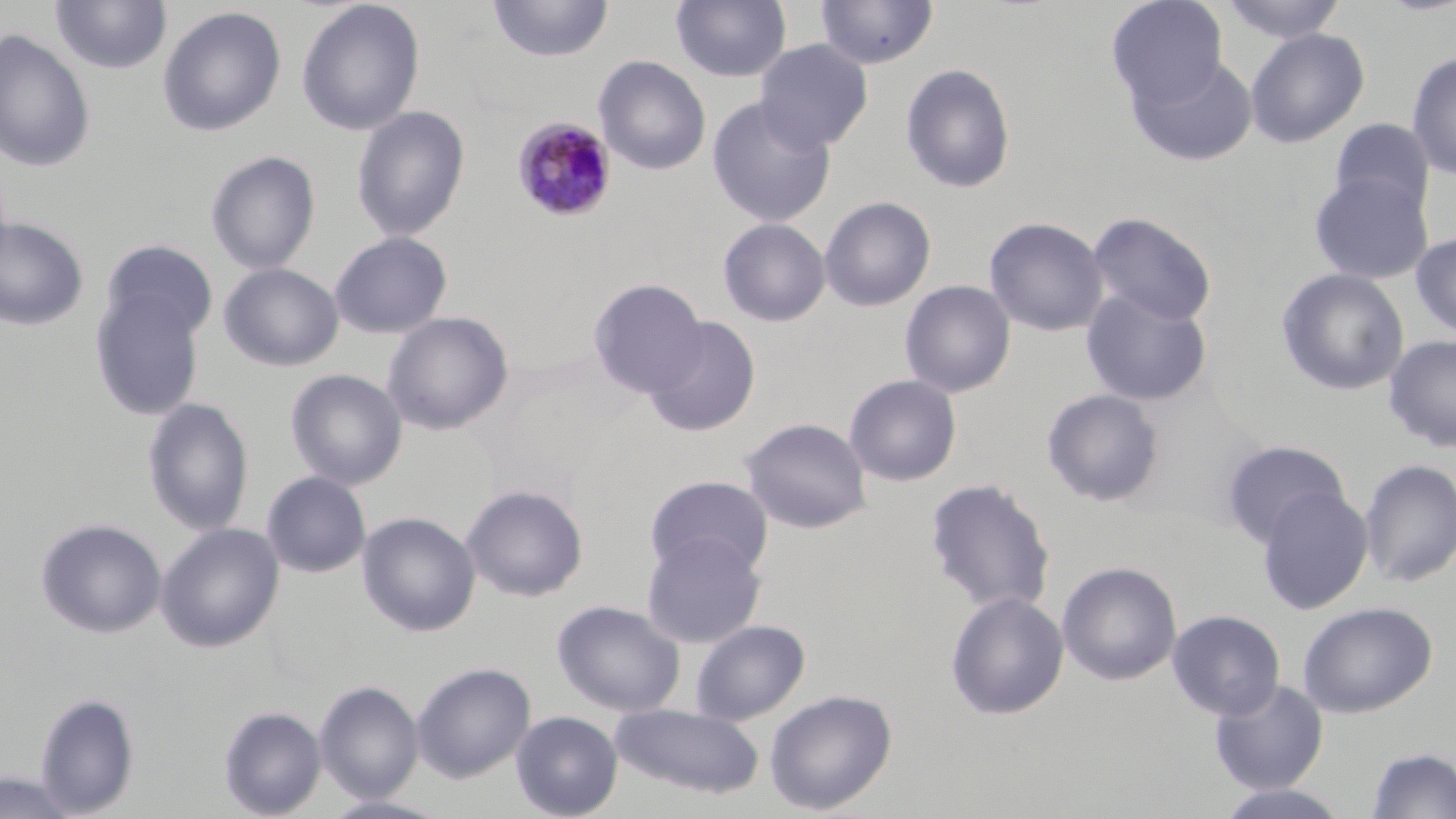

{
  "slide_level_diagnosis": "Plasmodium malariae",
  "magnification": "1000x",
  "field_of_view": "one of a larger specimen",
  "plasmodium_malariae_infected_red_blood_cell_locations": "approximate bounding boxes as named x1/y1/x2/y2 corners in pixels: (x1=512, y1=116, x2=618, y2=223)",
  "uninfected_red_blood_cell_locations": "approximate bounding boxes as named x1/y1/x2/y2 corners in pixels: (x1=488, y1=0, x2=613, y2=62), (x1=814, y1=0, x2=938, y2=70), (x1=1106, y1=0, x2=1229, y2=109), (x1=50, y1=1, x2=172, y2=75), (x1=296, y1=1, x2=425, y2=135), (x1=671, y1=1, x2=792, y2=82), (x1=1221, y1=1, x2=1347, y2=44), (x1=157, y1=6, x2=287, y2=137), (x1=1245, y1=27, x2=1369, y2=148), (x1=0, y1=28, x2=95, y2=174), (x1=755, y1=40, x2=873, y2=152), (x1=1407, y1=51, x2=1456, y2=179), (x1=1128, y1=53, x2=1258, y2=167), (x1=594, y1=55, x2=711, y2=175), (x1=900, y1=62, x2=1016, y2=194), (x1=707, y1=96, x2=836, y2=227), (x1=351, y1=105, x2=470, y2=242), (x1=1329, y1=118, x2=1436, y2=218), (x1=205, y1=150, x2=320, y2=274), (x1=1309, y1=172, x2=1433, y2=284), (x1=819, y1=196, x2=936, y2=310), (x1=1087, y1=212, x2=1217, y2=326), (x1=0, y1=217, x2=89, y2=331), (x1=984, y1=217, x2=1109, y2=336), (x1=718, y1=218, x2=830, y2=327), (x1=329, y1=231, x2=452, y2=339), (x1=1410, y1=232, x2=1456, y2=340), (x1=101, y1=240, x2=218, y2=344), (x1=219, y1=263, x2=343, y2=372), (x1=1276, y1=268, x2=1410, y2=396), (x1=588, y1=278, x2=708, y2=398), (x1=899, y1=280, x2=1016, y2=398), (x1=90, y1=288, x2=206, y2=421), (x1=1081, y1=289, x2=1212, y2=407), (x1=382, y1=311, x2=514, y2=435), (x1=645, y1=316, x2=761, y2=437), (x1=1384, y1=335, x2=1456, y2=452), (x1=286, y1=369, x2=407, y2=490), (x1=844, y1=374, x2=962, y2=487), (x1=1042, y1=389, x2=1165, y2=507), (x1=142, y1=397, x2=255, y2=536), (x1=739, y1=417, x2=872, y2=534), (x1=1220, y1=439, x2=1350, y2=547), (x1=1359, y1=459, x2=1456, y2=587), (x1=261, y1=471, x2=371, y2=578), (x1=645, y1=475, x2=774, y2=579), (x1=925, y1=478, x2=1056, y2=615), (x1=461, y1=484, x2=588, y2=602), (x1=1256, y1=486, x2=1374, y2=615), (x1=357, y1=512, x2=481, y2=636), (x1=36, y1=518, x2=167, y2=639), (x1=155, y1=522, x2=285, y2=653), (x1=641, y1=531, x2=766, y2=648), (x1=1057, y1=561, x2=1182, y2=686), (x1=945, y1=591, x2=1069, y2=720), (x1=552, y1=599, x2=686, y2=717), (x1=1297, y1=601, x2=1438, y2=718), (x1=1167, y1=609, x2=1285, y2=720), (x1=691, y1=619, x2=810, y2=725), (x1=412, y1=662, x2=536, y2=782), (x1=1208, y1=678, x2=1329, y2=794), (x1=314, y1=680, x2=424, y2=803), (x1=765, y1=689, x2=898, y2=815), (x1=34, y1=692, x2=140, y2=816), (x1=609, y1=703, x2=765, y2=800), (x1=219, y1=706, x2=326, y2=818), (x1=511, y1=710, x2=623, y2=819), (x1=1364, y1=747, x2=1456, y2=818), (x1=0, y1=771, x2=80, y2=818), (x1=1213, y1=783, x2=1352, y2=819), (x1=319, y1=794, x2=453, y2=819)",
  "preparation": "thin blood film",
  "image_size": "1456×819 pixels",
  "stain": "May-Grünwald-Giemsa",
  "modality": "light microscopy"
}